Assess this cell for malaria.
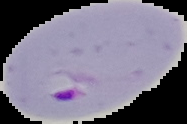

It is parasitized.

Segmented cell region on a black background. From a thin blood smear. Image is 187×124 pixels.